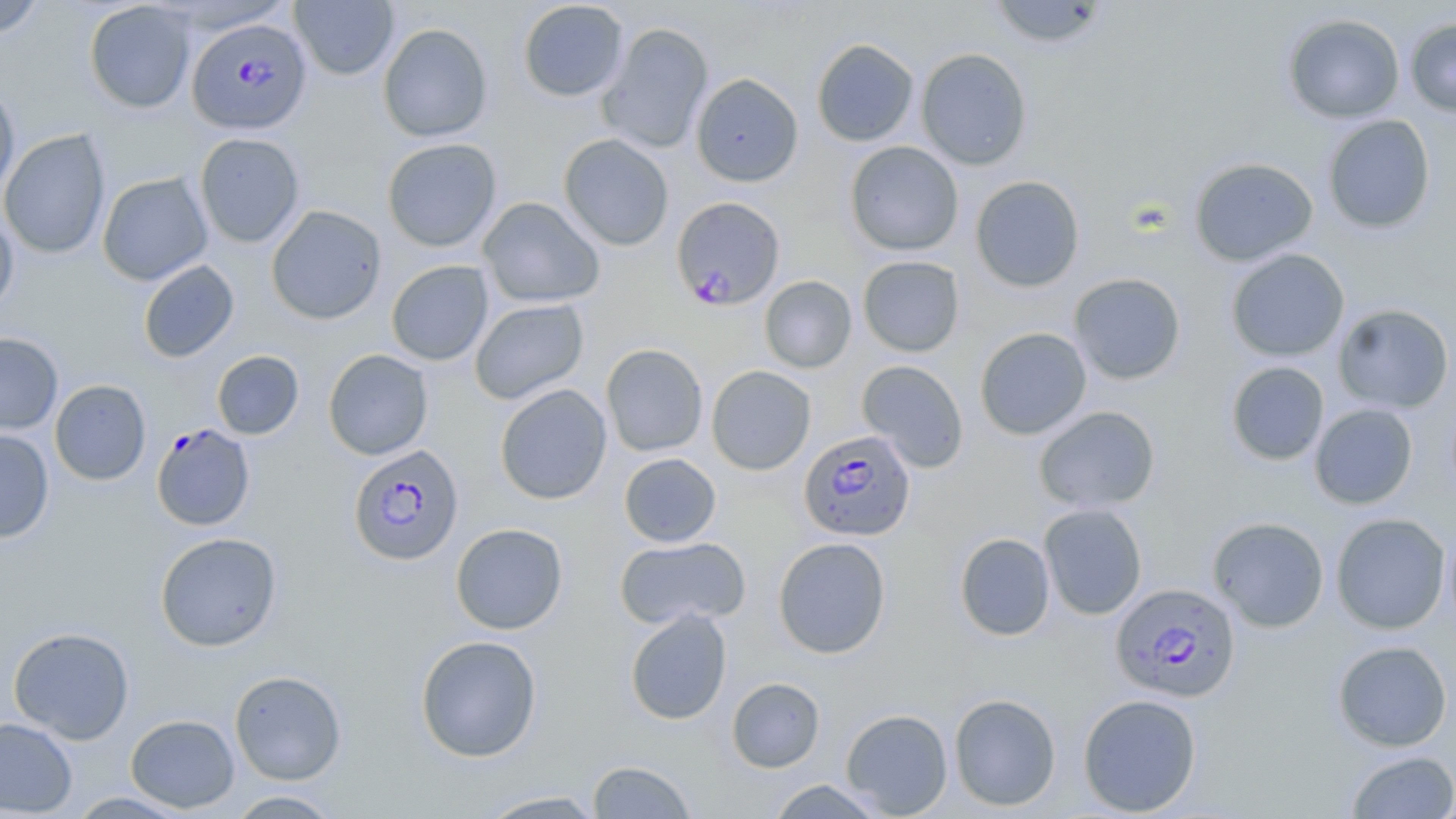
Approximate bounding boxes as (x1,y1)-(x2,y2) corner pairs in pixels. Plasmodium falciparum-infected red blood cell locations: (187,18)-(312,134), (671,196)-(786,309), (151,423)-(256,531), (799,429)-(916,541), (349,444)-(464,567), (1111,582)-(1241,702). Uninfected red blood cell locations: (290,0)-(399,80), (987,0)-(1111,49), (0,1)-(46,38), (84,1)-(196,114), (517,1)-(629,102), (1282,13)-(1405,124), (1404,17)-(1456,117), (598,22)-(714,153), (378,23)-(493,142), (811,38)-(919,146), (916,48)-(1032,170), (690,73)-(804,187), (0,85)-(20,199), (1322,114)-(1436,234), (0,129)-(111,259), (195,133)-(305,248), (558,134)-(674,251), (382,138)-(502,252), (844,141)-(964,256), (1189,157)-(1319,266), (97,172)-(213,285), (970,175)-(1085,292), (478,196)-(605,308), (266,205)-(387,325), (0,210)-(19,316), (1226,249)-(1350,362), (857,255)-(965,357), (137,260)-(239,363), (386,260)-(493,366), (1069,272)-(1186,385), (759,275)-(857,373), (470,299)-(589,404), (1333,303)-(1455,414), (974,327)-(1092,440), (0,332)-(63,435), (601,343)-(709,457), (323,349)-(433,460), (211,350)-(304,439), (857,359)-(969,473), (1226,361)-(1330,466), (706,366)-(816,475), (49,379)-(151,485), (494,383)-(612,505), (1309,403)-(1418,509), (1033,405)-(1161,514), (0,429)-(55,543), (619,453)-(721,547), (1039,503)-(1148,620), (1330,513)-(1451,634), (1207,516)-(1330,633), (1444,521)-(1456,637), (450,523)-(568,634), (155,532)-(282,652), (954,532)-(1056,641), (615,536)-(751,630), (772,537)-(891,659), (625,609)-(732,725), (8,626)-(135,744), (414,635)-(543,762), (1332,640)-(1453,752), (229,669)-(347,785), (727,677)-(825,772), (948,692)-(1061,811), (1077,693)-(1202,816), (840,708)-(953,817), (125,714)-(240,813), (0,717)-(77,817), (1346,750)-(1456,818), (586,759)-(698,818), (765,779)-(889,818), (225,789)-(346,818), (474,789)-(609,818), (67,791)-(191,818). Slide-level diagnosis: Plasmodium falciparum. May-Grünwald-Giemsa stain. Captured at 1000x magnification. Thin blood film. Image is 1456×819 pixels. Single field of view. Optical microscopy.